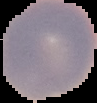
preparation: thin blood smear
image_type: segmented cell region with the area outside set to black
result: negative for Plasmodium parasites
image_size: 97×103 pixels